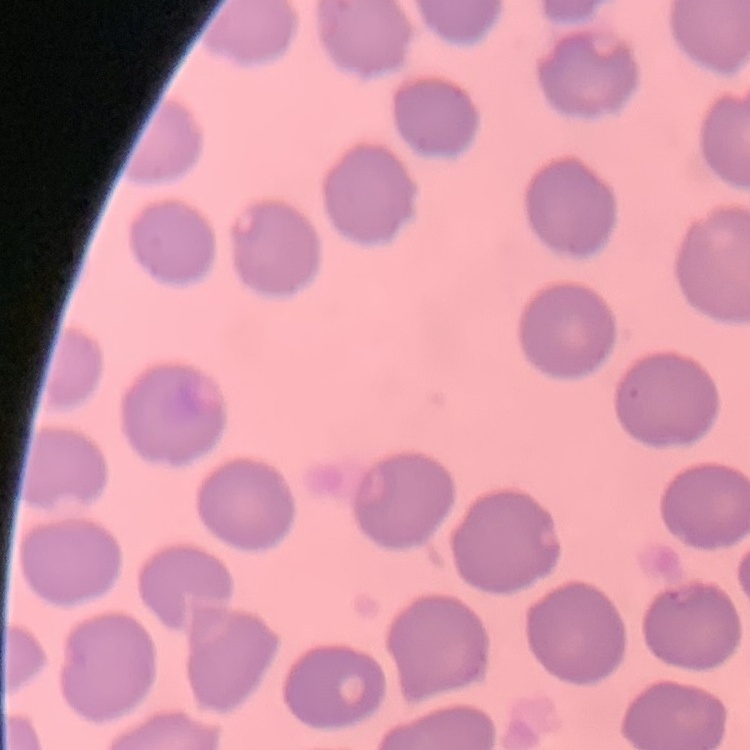
The erythrocytes show no rouleaux formation. Field's or Giemsa stain. One tile cut from a larger photomicrograph. Thin blood smear.